Describe the morphology of the red blood cells.
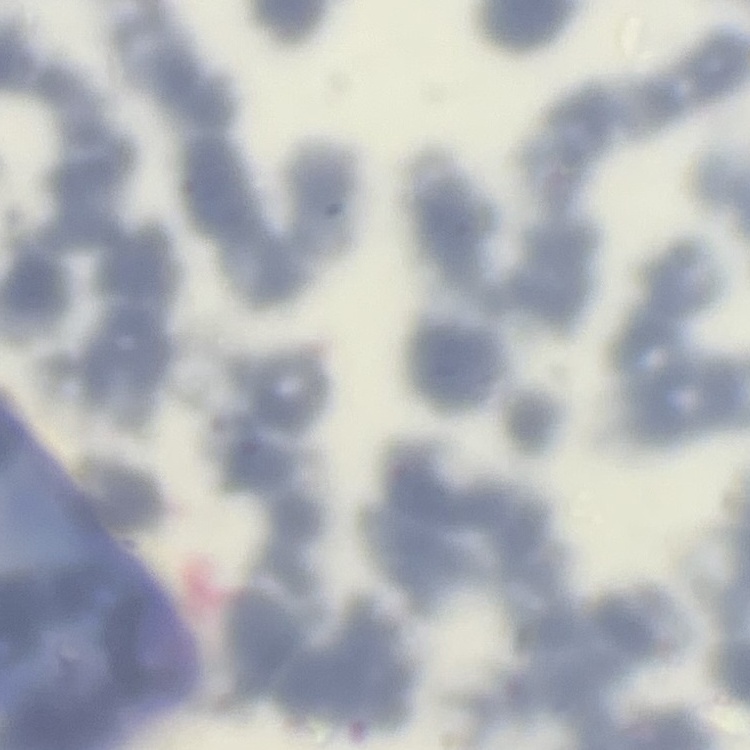
Rouleaux formation.

Stained with either Field's or Giemsa. Thin blood film. Square crop of a larger photomicrograph.